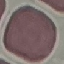

Result: negative for malaria parasites. Cell patch, automatically extracted from a larger field of view and resized to 64 × 64 pixels. Giemsa stain. Photographed with a smartphone camera at the microscope eyepiece. Thin blood film.